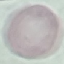 Result: no malaria parasites detected. Thin smear of blood. Photographed with a smartphone camera at the microscope eyepiece. Automatically extracted cell patch, resized to 64 × 64 pixels. Giemsa stain.